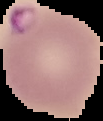
image type = segmented cell region on a black background
image size = 103×121 pixels
preparation = thin blood film
result = Plasmodium parasites detected